Classify this cell by malaria status.
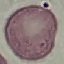
Uninfected.

preparation = thin blood smear
stain = Giemsa
capture = smartphone camera at the microscope eyepiece
image type = automatically extracted cell patch, resized to 64 × 64 pixels